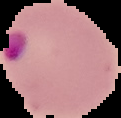

Image is 121×118 pixels. Segmented cell region on a black background. From a thin blood smear. Result: malaria parasites detected.